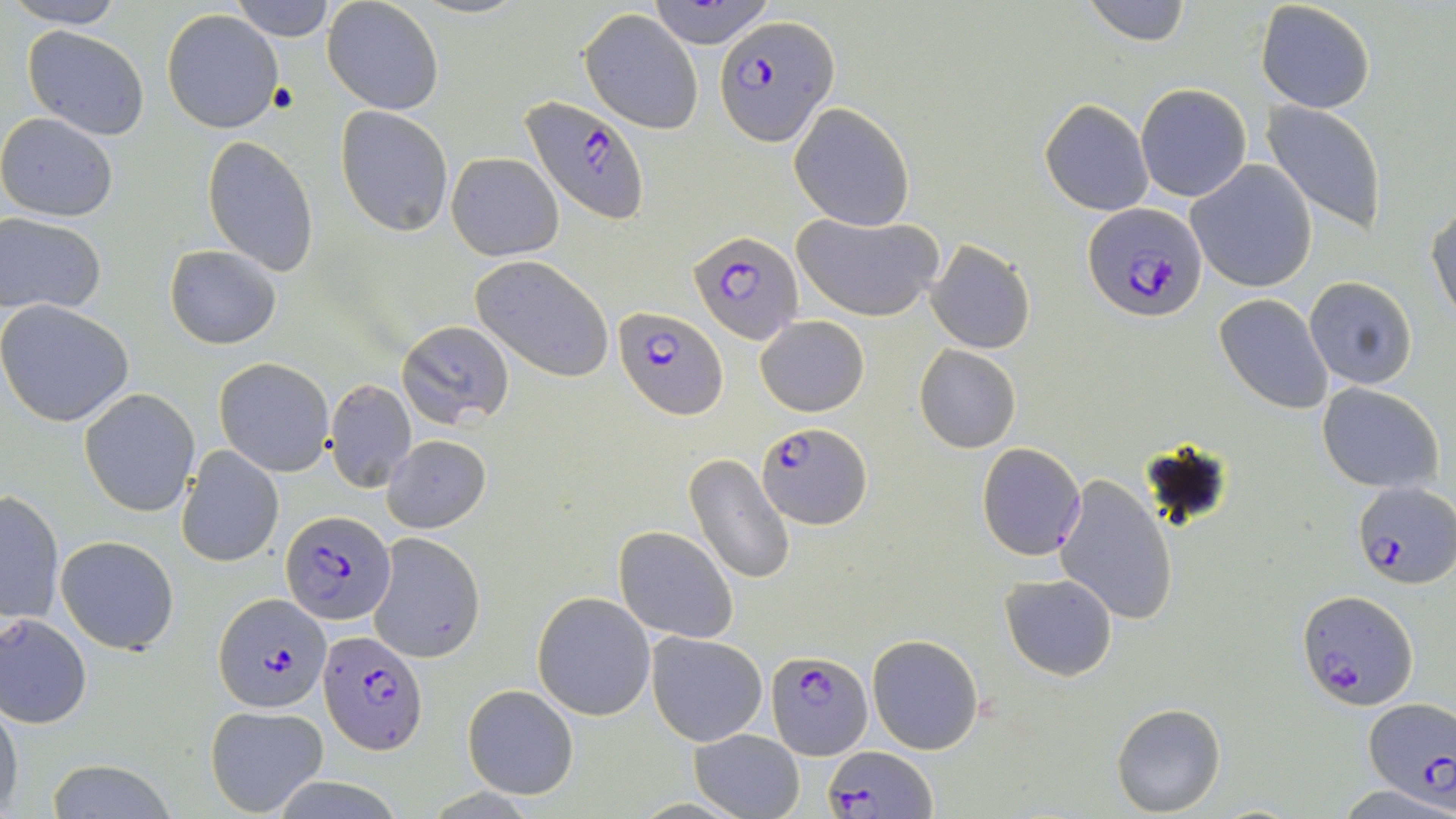

slide-level diagnosis = Plasmodium falciparum
magnification = 1000x
image size = 1456×819 pixels
modality = optical microscopy
uninfected red blood cell locations = approximate bounding boxes as [x1, y1, x2, y2] in pixels: [11, 0, 127, 27], [228, 0, 338, 39], [647, 0, 780, 49], [1080, 0, 1193, 47], [1255, 0, 1376, 113], [322, 2, 443, 116], [163, 9, 283, 133], [580, 9, 705, 134], [22, 25, 150, 139], [1135, 84, 1251, 202], [1041, 99, 1154, 216], [1261, 101, 1388, 234], [788, 102, 915, 230], [336, 106, 454, 237], [0, 112, 119, 222], [203, 136, 319, 274], [446, 152, 564, 261], [1188, 160, 1317, 293], [1427, 204, 1456, 328], [793, 211, 945, 322], [1, 214, 106, 314], [926, 238, 1036, 354], [166, 246, 283, 349], [470, 257, 615, 382], [1304, 276, 1417, 389], [1214, 294, 1334, 415], [0, 301, 135, 426], [756, 316, 869, 416], [398, 320, 515, 427], [914, 345, 1022, 453], [215, 357, 334, 476], [325, 379, 416, 491], [1317, 382, 1443, 491], [79, 388, 200, 516], [384, 435, 491, 533], [976, 443, 1086, 561], [177, 446, 284, 568], [684, 453, 796, 587], [1054, 474, 1179, 626], [0, 490, 66, 626], [614, 527, 739, 643], [370, 532, 485, 663], [56, 535, 180, 655], [1001, 573, 1118, 680], [532, 593, 654, 719], [1, 612, 93, 728], [645, 631, 767, 746], [867, 635, 983, 755], [463, 684, 578, 798], [0, 694, 23, 819], [1112, 702, 1226, 816], [206, 703, 328, 815], [691, 728, 804, 818], [43, 762, 180, 819], [1339, 783, 1455, 818]
field of view = one of a larger specimen
preparation = thin blood smear
stain = May-Grünwald-Giemsa
Plasmodium falciparum-infected red blood cell locations = approximate bounding boxes as [x1, y1, x2, y2] in pixels: [718, 16, 838, 145], [519, 94, 649, 224], [1083, 202, 1210, 324], [690, 230, 800, 345], [612, 306, 728, 419], [756, 422, 870, 527], [1351, 481, 1454, 587], [281, 509, 396, 624], [1297, 589, 1418, 712], [215, 593, 331, 713], [318, 628, 427, 752], [764, 649, 871, 760], [1363, 699, 1455, 802], [825, 746, 934, 818]